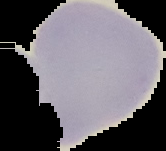 Segmented cell region on a black background. Result: no Plasmodium parasites seen. Image is 166×151 pixels. From a thin blood smear.